Point out each Plasmodium parasite.
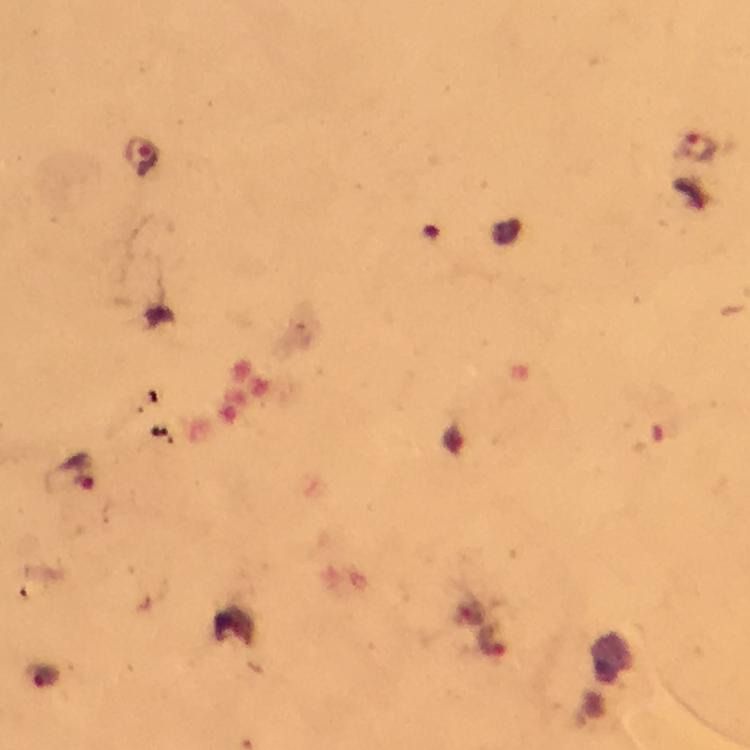

Approximate centers as [x, y] in pixels.
Plasmodium parasites: [697, 149], [141, 156], [81, 472], [492, 641].

context = from a malaria diagnostic workup
preparation = thick blood smear
magnification = 100x
cropped from = a single field of view
stain = Giemsa
immersion oil = used
capture = smartphone camera through the microscope
image size = 750×750 pixels